Name the parasite shown.
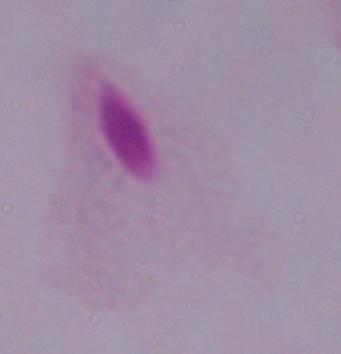
This is a trichomonad.

Summary:
  - Modality: photomicrograph
  - Magnification: 1000x